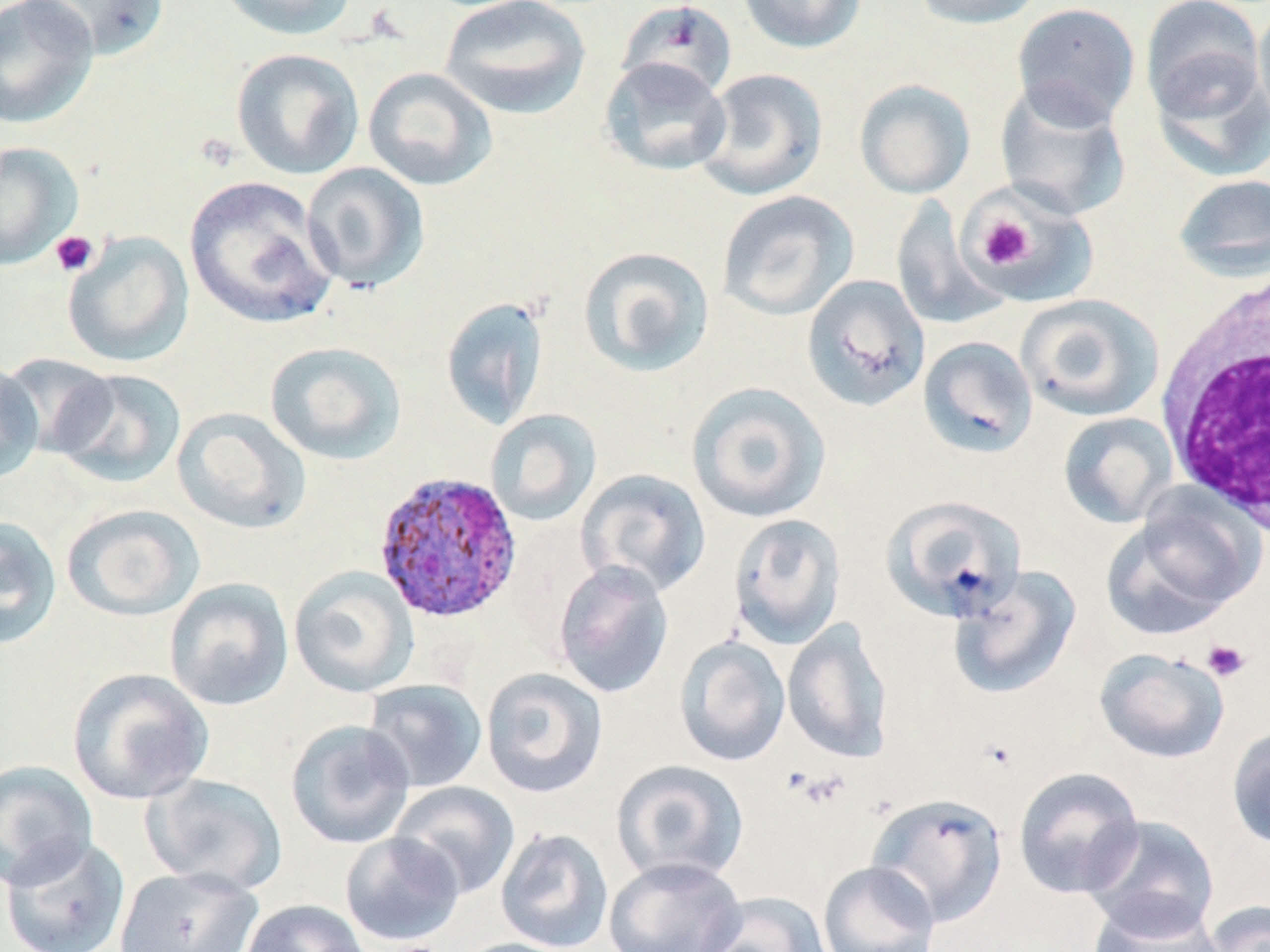 Approximate bounding boxes as named x1/y1/x2/y2 corners in pixels. Uninfected red blood cell locations: (x1=0, y1=0, x2=99, y2=129), (x1=18, y1=0, x2=171, y2=60), (x1=214, y1=0, x2=358, y2=40), (x1=439, y1=0, x2=591, y2=120), (x1=737, y1=0, x2=867, y2=54), (x1=912, y1=0, x2=1045, y2=29), (x1=1140, y1=0, x2=1266, y2=121), (x1=618, y1=1, x2=736, y2=100), (x1=1011, y1=2, x2=1141, y2=129), (x1=1253, y1=4, x2=1270, y2=132), (x1=231, y1=48, x2=364, y2=180), (x1=599, y1=56, x2=732, y2=177), (x1=1149, y1=57, x2=1270, y2=182), (x1=363, y1=66, x2=498, y2=191), (x1=694, y1=67, x2=829, y2=201), (x1=854, y1=79, x2=976, y2=199), (x1=994, y1=82, x2=1131, y2=220), (x1=0, y1=141, x2=83, y2=270), (x1=301, y1=161, x2=430, y2=293), (x1=1172, y1=173, x2=1270, y2=280), (x1=184, y1=175, x2=339, y2=330), (x1=717, y1=190, x2=859, y2=321), (x1=969, y1=191, x2=1096, y2=308), (x1=891, y1=197, x2=1007, y2=330), (x1=62, y1=232, x2=195, y2=368), (x1=576, y1=245, x2=716, y2=378), (x1=801, y1=274, x2=930, y2=412), (x1=1016, y1=294, x2=1164, y2=422), (x1=440, y1=295, x2=550, y2=431), (x1=918, y1=336, x2=1038, y2=459), (x1=265, y1=341, x2=407, y2=465), (x1=2, y1=353, x2=118, y2=458), (x1=0, y1=357, x2=44, y2=484), (x1=52, y1=369, x2=187, y2=489), (x1=685, y1=381, x2=832, y2=523), (x1=173, y1=407, x2=311, y2=535), (x1=485, y1=409, x2=602, y2=527), (x1=1058, y1=412, x2=1177, y2=528), (x1=576, y1=468, x2=711, y2=598), (x1=881, y1=495, x2=1027, y2=623), (x1=1103, y1=495, x2=1260, y2=638), (x1=61, y1=504, x2=205, y2=622), (x1=728, y1=513, x2=846, y2=649), (x1=0, y1=515, x2=62, y2=650), (x1=552, y1=560, x2=674, y2=699), (x1=288, y1=565, x2=420, y2=697), (x1=948, y1=566, x2=1081, y2=700), (x1=164, y1=578, x2=294, y2=711), (x1=782, y1=618, x2=894, y2=763), (x1=675, y1=635, x2=791, y2=767), (x1=1094, y1=648, x2=1230, y2=764), (x1=66, y1=667, x2=214, y2=805), (x1=480, y1=667, x2=608, y2=798), (x1=362, y1=679, x2=488, y2=794), (x1=285, y1=719, x2=415, y2=849), (x1=1226, y1=724, x2=1270, y2=850), (x1=0, y1=759, x2=97, y2=890), (x1=611, y1=759, x2=750, y2=885), (x1=1013, y1=766, x2=1145, y2=899), (x1=143, y1=772, x2=288, y2=895), (x1=388, y1=781, x2=520, y2=900), (x1=866, y1=792, x2=1008, y2=927), (x1=1082, y1=815, x2=1221, y2=938), (x1=495, y1=827, x2=614, y2=952), (x1=340, y1=832, x2=465, y2=947), (x1=1, y1=834, x2=131, y2=952), (x1=603, y1=856, x2=746, y2=952), (x1=817, y1=860, x2=941, y2=952), (x1=112, y1=866, x2=263, y2=952), (x1=699, y1=891, x2=831, y2=952), (x1=1086, y1=895, x2=1224, y2=952), (x1=240, y1=899, x2=370, y2=952), (x1=1202, y1=899, x2=1270, y2=952), (x1=451, y1=937, x2=583, y2=952). Platelet locations: (x1=976, y1=216, x2=1035, y2=270), (x1=49, y1=231, x2=98, y2=277), (x1=1202, y1=639, x2=1251, y2=683), (x1=789, y1=768, x2=852, y2=810). Plasmodium ovale-infected red blood cell locations: (x1=373, y1=471, x2=523, y2=624). White blood cell locations: (x1=1156, y1=267, x2=1270, y2=539). Slide-level diagnosis: Plasmodium ovale. Light microscopy. Single field of view. 1000x magnification. Thin blood film. May-Grünwald-Giemsa stain. Image is 1270×952 pixels.